Report the malaria status.
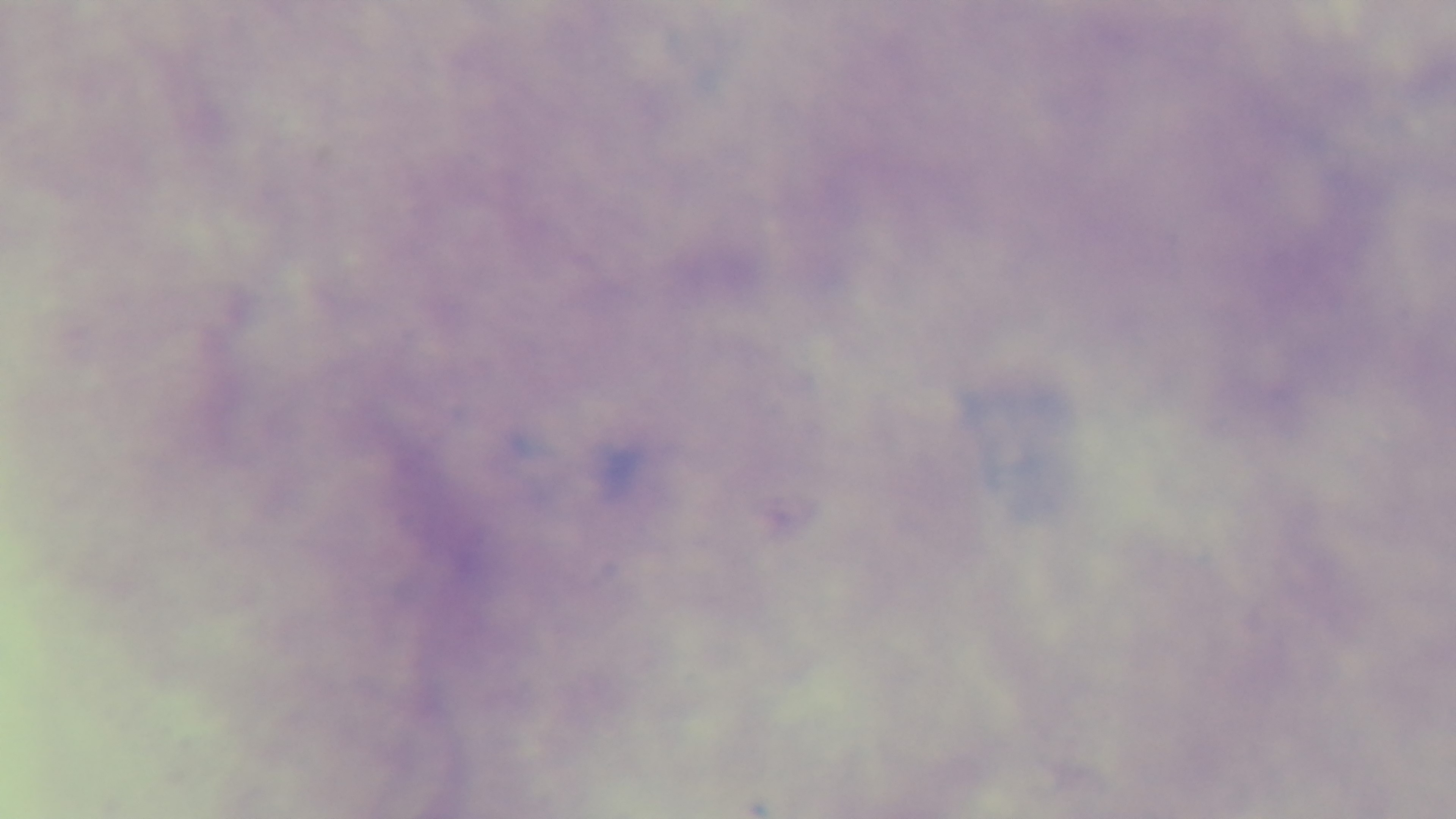

Negative.

field of view = one from the slide
capture = mounted 4K digital camera
objective = 100x oil immersion
preparation = thick blood film
modality = light microscopy
stain = Giemsa